Outline each blood parasite and name the species.
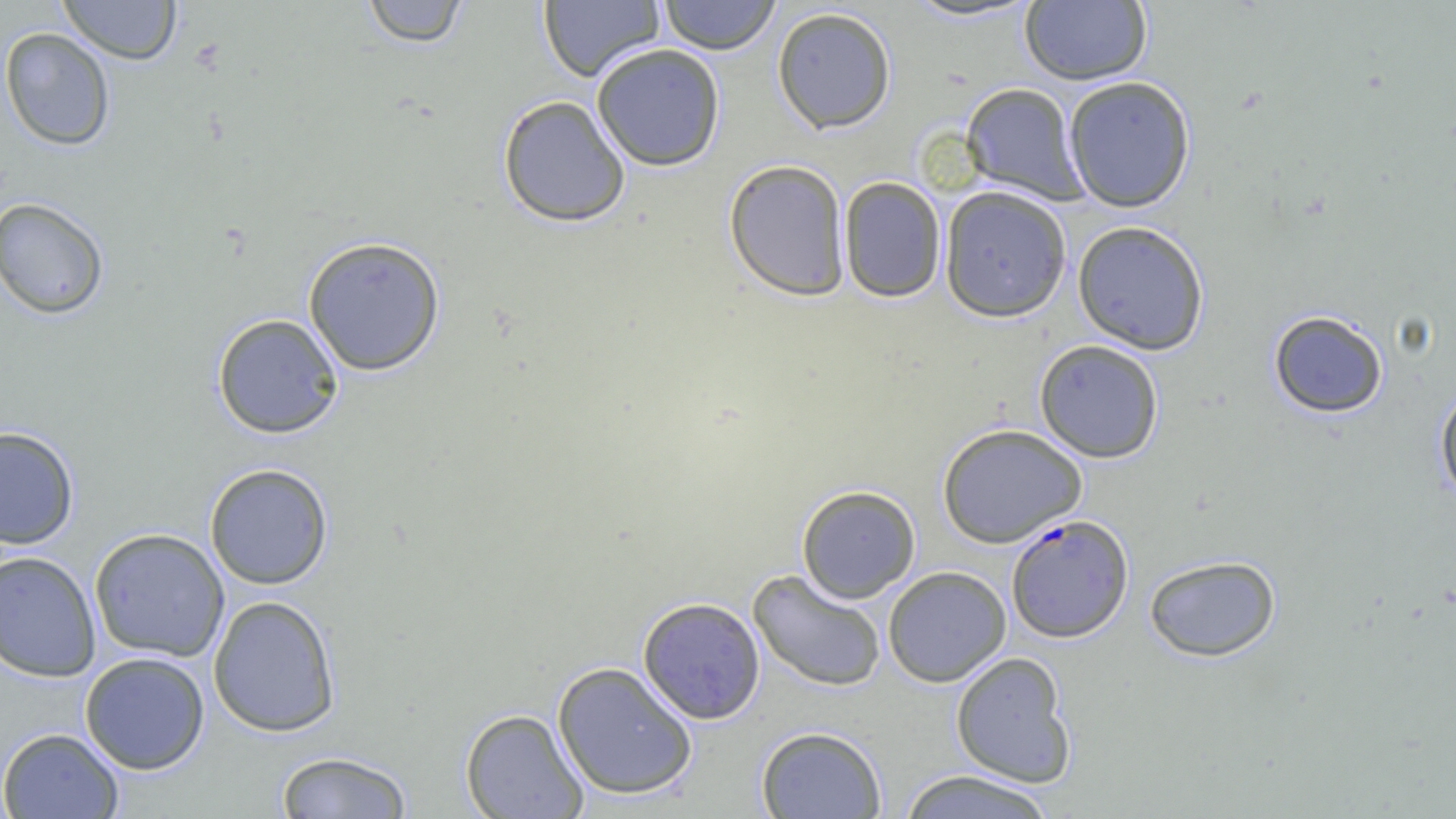

Approximate bounding boxes as (x1, y1, x2, y2) in pixels.
Plasmodium falciparum-infected red blood cells: (1006, 513, 1134, 642).
No Plasmodium ovale, Plasmodium malariae, Plasmodium vivax, Babesia divergens, or Trypanosoma brucei observed.

Uninfected red blood cell locations: (58, 0, 182, 65), (359, 0, 471, 48), (658, 0, 781, 55), (1020, 0, 1152, 85), (537, 1, 665, 82), (899, 1, 1045, 24), (772, 6, 897, 134), (0, 27, 116, 151), (591, 42, 726, 171), (1063, 75, 1196, 213), (960, 82, 1087, 204), (497, 94, 631, 228), (723, 158, 851, 302), (838, 176, 947, 303), (938, 185, 1072, 322), (0, 197, 110, 319), (1072, 220, 1210, 355), (302, 235, 446, 376), (1268, 309, 1389, 418), (212, 312, 345, 439), (1034, 339, 1165, 463), (1433, 385, 1456, 506), (937, 423, 1087, 547), (0, 426, 80, 549), (204, 463, 334, 589), (796, 484, 921, 603), (88, 528, 230, 662), (0, 550, 102, 683), (1143, 554, 1281, 662), (883, 566, 1011, 687), (748, 569, 887, 692), (208, 595, 341, 737), (637, 596, 766, 724), (950, 651, 1077, 788), (79, 652, 210, 775), (552, 661, 698, 800), (460, 708, 589, 819), (756, 725, 888, 819), (0, 727, 125, 819), (274, 750, 414, 818), (896, 769, 1058, 819). Slide-level diagnosis: Plasmodium falciparum. One field of a larger specimen. Optical microscopy. Thin blood film. Image is 1456×819 pixels. 1000x magnification.